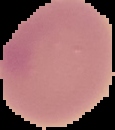
Summary:
  - Result: negative for malaria parasites
  - Image size: 115×130 pixels
  - Preparation: thin blood film
  - Image type: cell region segmented out of the field of view; surrounding area masked to black